Report the malaria status of this cell.
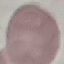

Uninfected.

Summary:
  - Stain: Giemsa
  - Capture: smartphone camera at the microscope eyepiece
  - Preparation: thin smear
  - Image type: automatically extracted cell patch, resized to 64 × 64 pixels